Classify this cell by malaria status.
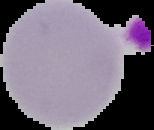
It is uninfected.

Image is 154×130 pixels. Segmented cell region on a black background. From a thin blood smear.